Name the cell type shown.
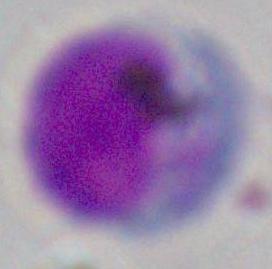

A leukocyte.

Summary:
  - Modality: micrograph
  - Magnification: 1000x